Classify this cell by malaria status.
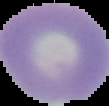
Uninfected.

image_type: cell region segmented out of the field of view; surrounding area masked to black
preparation: thin blood smear
image_size: 109×106 pixels